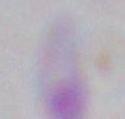

Summary:
  - Identification: Toxoplasma gondii
  - Modality: photomicrograph
  - Magnification: 1000x